Report the malaria status of this cell.
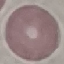

Uninfected.

Thin blood smear. Giemsa-stained preparation. Photographed with a smartphone camera at the microscope eyepiece. Cell patch, automatically extracted from a larger field of view and resized to 64 × 64 pixels.